Report the malaria status of this cell.
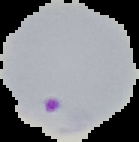

It is parasitized.

From a thin blood film. Image is 139×142 pixels. The area outside the segmented cell region is set to black.